Classify this cell by malaria status.
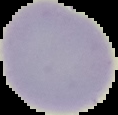
It is uninfected.

Summary:
  - Preparation: thin blood film
  - Image size: 118×115 pixels
  - Image type: segmented cell region with the area outside set to black